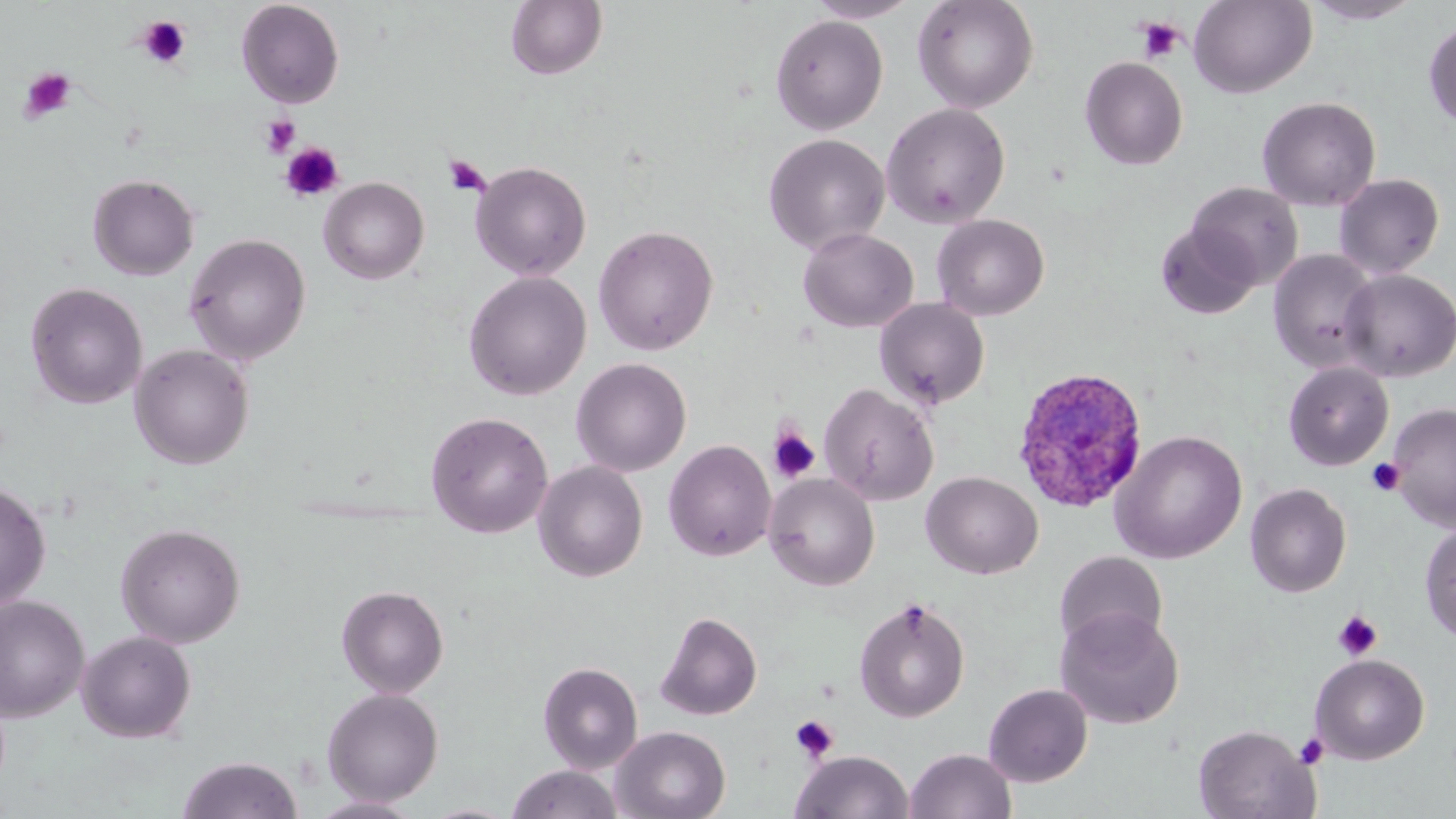 Approximate bounding boxes as [x1, y1, x2, y2] in pixels. Platelet locations: [137, 16, 190, 68], [1136, 18, 1185, 63], [19, 66, 78, 124], [259, 114, 301, 157], [279, 142, 344, 203], [443, 154, 490, 197], [768, 426, 820, 484], [1366, 458, 1405, 496], [1333, 609, 1382, 661], [790, 714, 838, 762], [1294, 733, 1329, 768]. Plasmodium ovale-infected red blood cell locations: [1012, 366, 1149, 514]. Uninfected red blood cell locations: [236, 0, 345, 108], [806, 0, 920, 23], [912, 0, 1039, 114], [1188, 0, 1317, 98], [1304, 0, 1424, 25], [506, 1, 608, 81], [770, 13, 888, 135], [1423, 17, 1456, 132], [1079, 56, 1188, 170], [1257, 96, 1381, 211], [880, 103, 1011, 229], [763, 134, 890, 255], [471, 160, 592, 281], [87, 173, 199, 280], [1334, 173, 1445, 279], [319, 177, 429, 285], [1187, 181, 1303, 289], [932, 214, 1049, 320], [1155, 222, 1261, 320], [593, 224, 719, 355], [798, 227, 918, 332], [184, 232, 311, 365], [1268, 249, 1381, 372], [1339, 269, 1456, 382], [463, 271, 591, 401], [25, 281, 148, 410], [875, 298, 991, 409], [130, 343, 254, 470], [571, 358, 691, 477], [1284, 361, 1394, 471], [819, 382, 939, 505], [1388, 403, 1456, 531], [426, 411, 553, 538], [1111, 430, 1248, 564], [664, 439, 776, 561], [533, 461, 648, 582], [921, 471, 1043, 579], [764, 473, 880, 591], [0, 480, 51, 611], [1245, 482, 1351, 598], [1419, 521, 1456, 643], [115, 523, 245, 647], [1054, 551, 1168, 653], [336, 585, 449, 698], [0, 595, 90, 722], [853, 597, 970, 723], [1055, 607, 1185, 730], [656, 611, 763, 721], [77, 630, 197, 743], [1310, 654, 1430, 764], [538, 661, 643, 773], [983, 683, 1093, 787], [322, 687, 444, 806], [1192, 724, 1319, 819], [611, 725, 730, 819], [905, 747, 1017, 819], [791, 749, 914, 818], [177, 755, 303, 819], [504, 764, 625, 819], [308, 796, 422, 818], [420, 802, 519, 818]. Slide-level diagnosis: Plasmodium ovale. One field of a larger specimen. Thin blood smear. Image is 1456×819 pixels. 1000x magnification. May-Grünwald-Giemsa-stained preparation. Light microscopy.